Locate and identify every blood parasite.
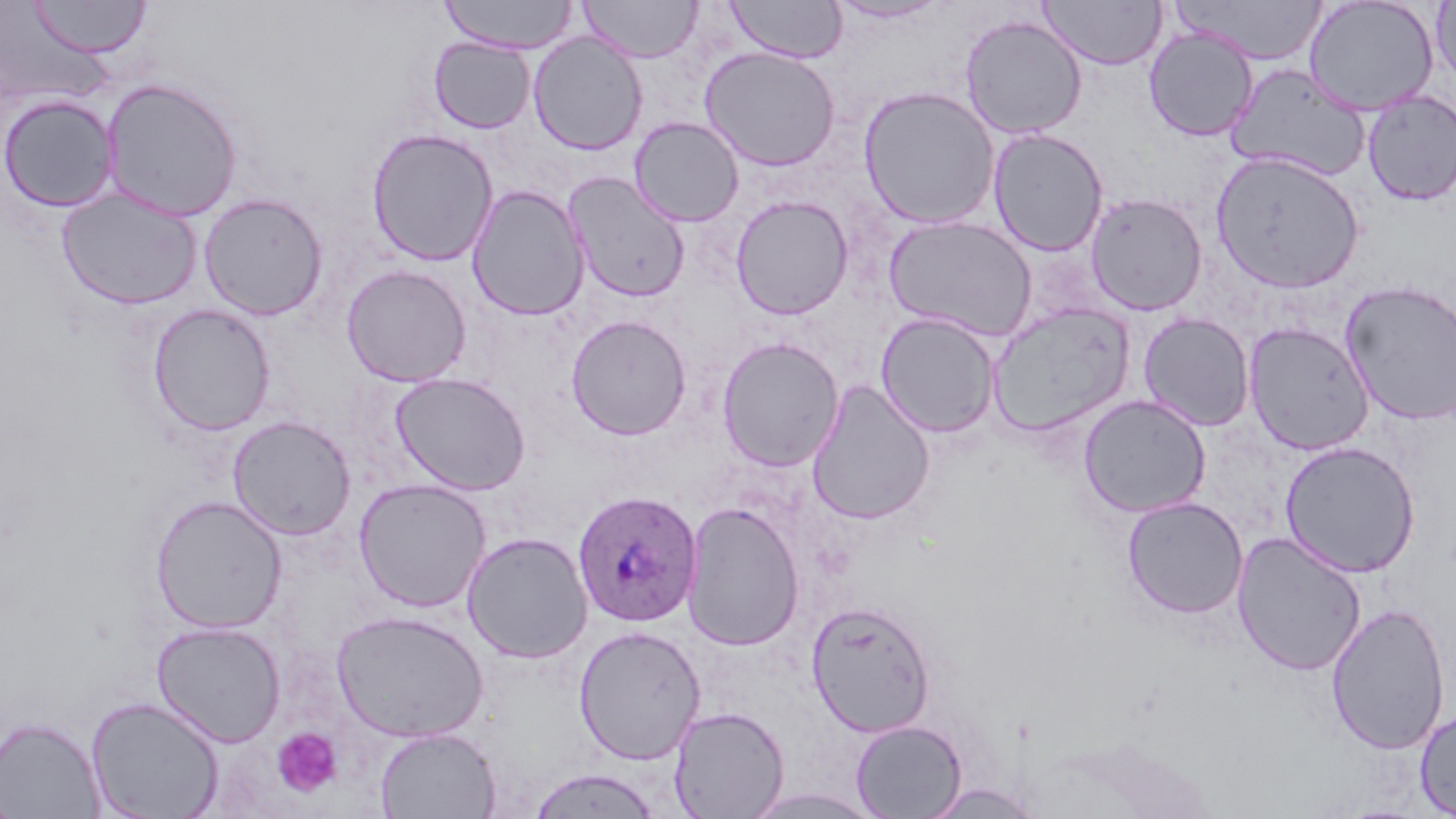
Approximate bounding boxes as named x1/y1/x2/y2 corners in pixels.
Plasmodium ovale-infected red blood cells: (x1=572, y1=490, x2=703, y2=628).
No Plasmodium falciparum, Plasmodium malariae, Plasmodium vivax, Babesia divergens, or Trypanosoma brucei observed.

slide-level diagnosis = Plasmodium ovale
modality = light microscopy
image size = 1456×819 pixels
magnification = 1000x
preparation = thin blood smear
platelet locations = approximate bounding boxes as named x1/y1/x2/y2 corners in pixels: (x1=272, y1=727, x2=343, y2=798)
uninfected red blood cell locations = approximate bounding boxes as named x1/y1/x2/y2 corners in pixels: (x1=28, y1=0, x2=151, y2=59), (x1=438, y1=0, x2=580, y2=53), (x1=578, y1=0, x2=703, y2=62), (x1=725, y1=0, x2=847, y2=63), (x1=1038, y1=0, x2=1167, y2=70), (x1=1303, y1=0, x2=1439, y2=115), (x1=827, y1=1, x2=951, y2=25), (x1=1171, y1=1, x2=1329, y2=65), (x1=1430, y1=1, x2=1456, y2=88), (x1=960, y1=14, x2=1088, y2=139), (x1=1145, y1=27, x2=1258, y2=142), (x1=528, y1=32, x2=648, y2=155), (x1=429, y1=38, x2=535, y2=133), (x1=699, y1=46, x2=841, y2=171), (x1=1225, y1=64, x2=1371, y2=180), (x1=100, y1=77, x2=244, y2=221), (x1=858, y1=85, x2=1001, y2=230), (x1=1361, y1=89, x2=1456, y2=206), (x1=1, y1=94, x2=119, y2=213), (x1=629, y1=117, x2=744, y2=227), (x1=366, y1=128, x2=499, y2=267), (x1=987, y1=128, x2=1109, y2=257), (x1=1210, y1=151, x2=1365, y2=293), (x1=563, y1=171, x2=691, y2=304), (x1=466, y1=184, x2=590, y2=321), (x1=56, y1=189, x2=203, y2=310), (x1=1085, y1=191, x2=1208, y2=316), (x1=199, y1=193, x2=328, y2=321), (x1=730, y1=195, x2=854, y2=320), (x1=883, y1=216, x2=1038, y2=341), (x1=341, y1=264, x2=472, y2=387), (x1=1340, y1=281, x2=1456, y2=426), (x1=148, y1=303, x2=276, y2=437), (x1=985, y1=303, x2=1135, y2=438), (x1=875, y1=312, x2=1001, y2=438), (x1=1138, y1=312, x2=1256, y2=431), (x1=566, y1=315, x2=692, y2=440), (x1=1242, y1=322, x2=1375, y2=455), (x1=716, y1=336, x2=845, y2=472), (x1=390, y1=372, x2=530, y2=495), (x1=805, y1=380, x2=936, y2=526), (x1=1077, y1=394, x2=1212, y2=518), (x1=227, y1=415, x2=357, y2=540), (x1=1279, y1=441, x2=1421, y2=577), (x1=353, y1=478, x2=491, y2=612), (x1=149, y1=494, x2=287, y2=633), (x1=1122, y1=496, x2=1248, y2=619), (x1=682, y1=501, x2=805, y2=651), (x1=1231, y1=531, x2=1367, y2=677), (x1=462, y1=532, x2=593, y2=664), (x1=806, y1=601, x2=936, y2=736), (x1=1326, y1=603, x2=1451, y2=755), (x1=331, y1=609, x2=489, y2=742), (x1=151, y1=622, x2=286, y2=746), (x1=573, y1=625, x2=705, y2=765), (x1=86, y1=695, x2=226, y2=819), (x1=668, y1=705, x2=789, y2=818), (x1=1414, y1=708, x2=1456, y2=817), (x1=0, y1=715, x2=105, y2=819), (x1=850, y1=719, x2=966, y2=818), (x1=374, y1=726, x2=502, y2=819), (x1=527, y1=768, x2=663, y2=818), (x1=921, y1=783, x2=1044, y2=818), (x1=736, y1=787, x2=888, y2=819), (x1=0, y1=788, x2=23, y2=819)
stain = May-Grünwald-Giemsa
field of view = single